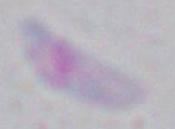 Captured at 1000x magnification. Micrograph. Toxoplasma gondii is seen.